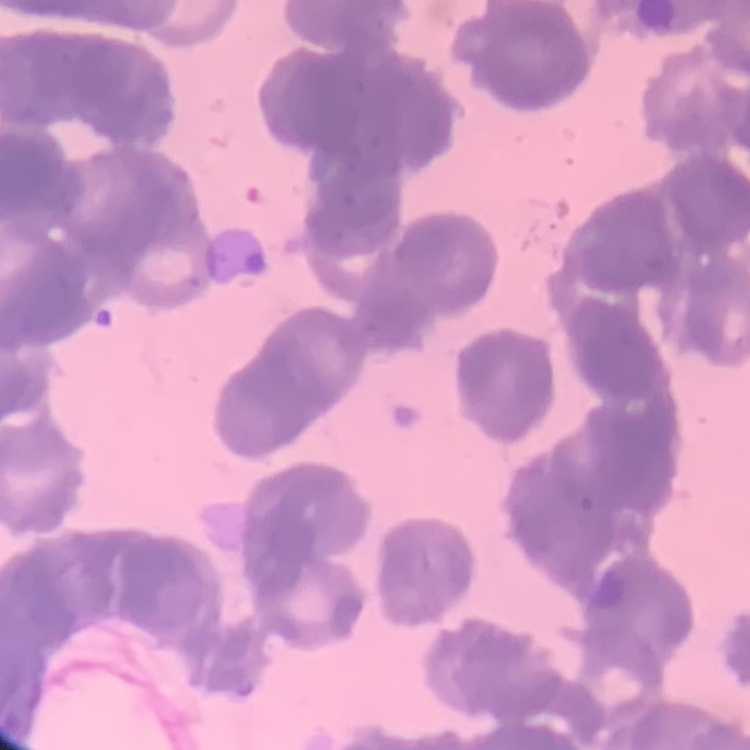

The red blood cells exhibit rouleaux formation. One tile cut from a larger photomicrograph. Thin blood film. Field's or Giemsa stain.